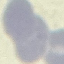

result = negative for malaria parasites
preparation = thin blood film
capture = smartphone camera at the microscope eyepiece
stain = Giemsa
image type = cell patch, automatically extracted from a larger field of view and resized to 64 × 64 pixels